Look for Plasmodium parasites.
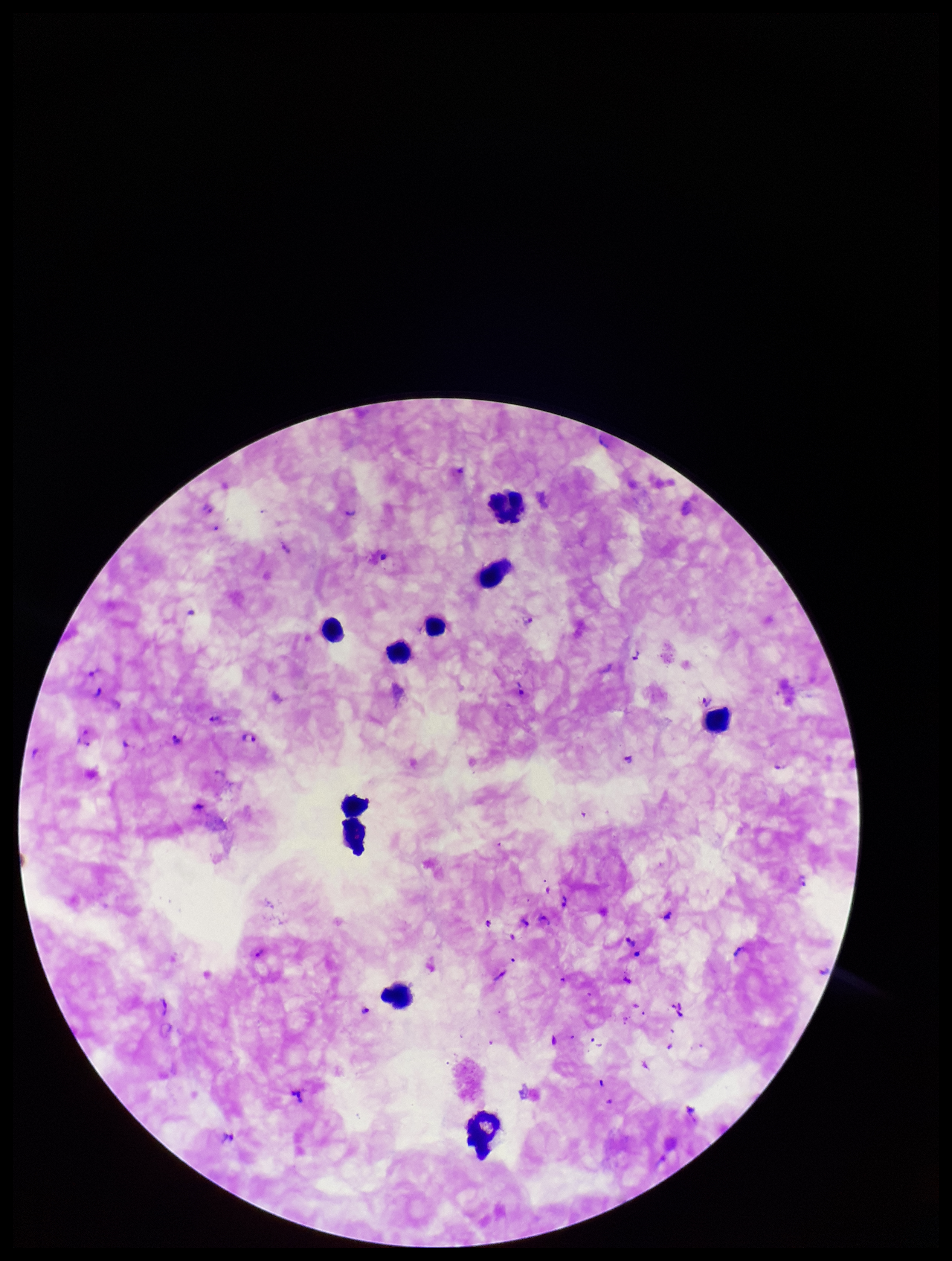
Seen.

stain: Giemsa
field_of_view: one from this slide
patient_malaria_status: positive
capture: smartphone photograph through the microscope eyepiece
preparation: thick
species_reported_for_this_patient: Plasmodium falciparum
parasite_count: 10
image_size: 952×1261 pixels
leukocyte_count: 9